Assess this cell for malaria.
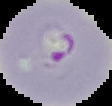

It is parasitized.

The area outside the segmented cell region is set to black. From a thin blood smear. Image is 112×106 pixels.